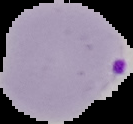 From a thin blood smear. Result: malaria parasites identified. The area outside the segmented cell region is set to black. Image is 133×124 pixels.